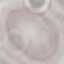 Result: no malaria parasites seen. Thin blood smear. Automatically extracted cell patch, resized to 64 × 64 pixels. Photographed with a smartphone camera at the microscope eyepiece. Giemsa stain.